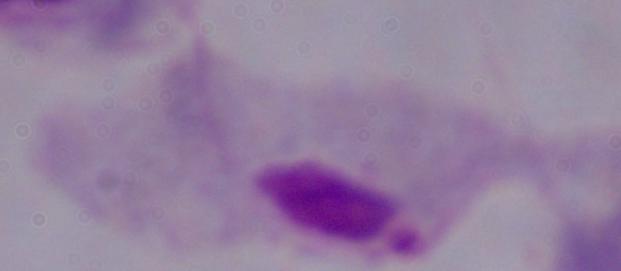 1000x magnification. A trichomonad is shown. Photomicrograph.